Locate every Plasmodium ovale-infected red blood cell.
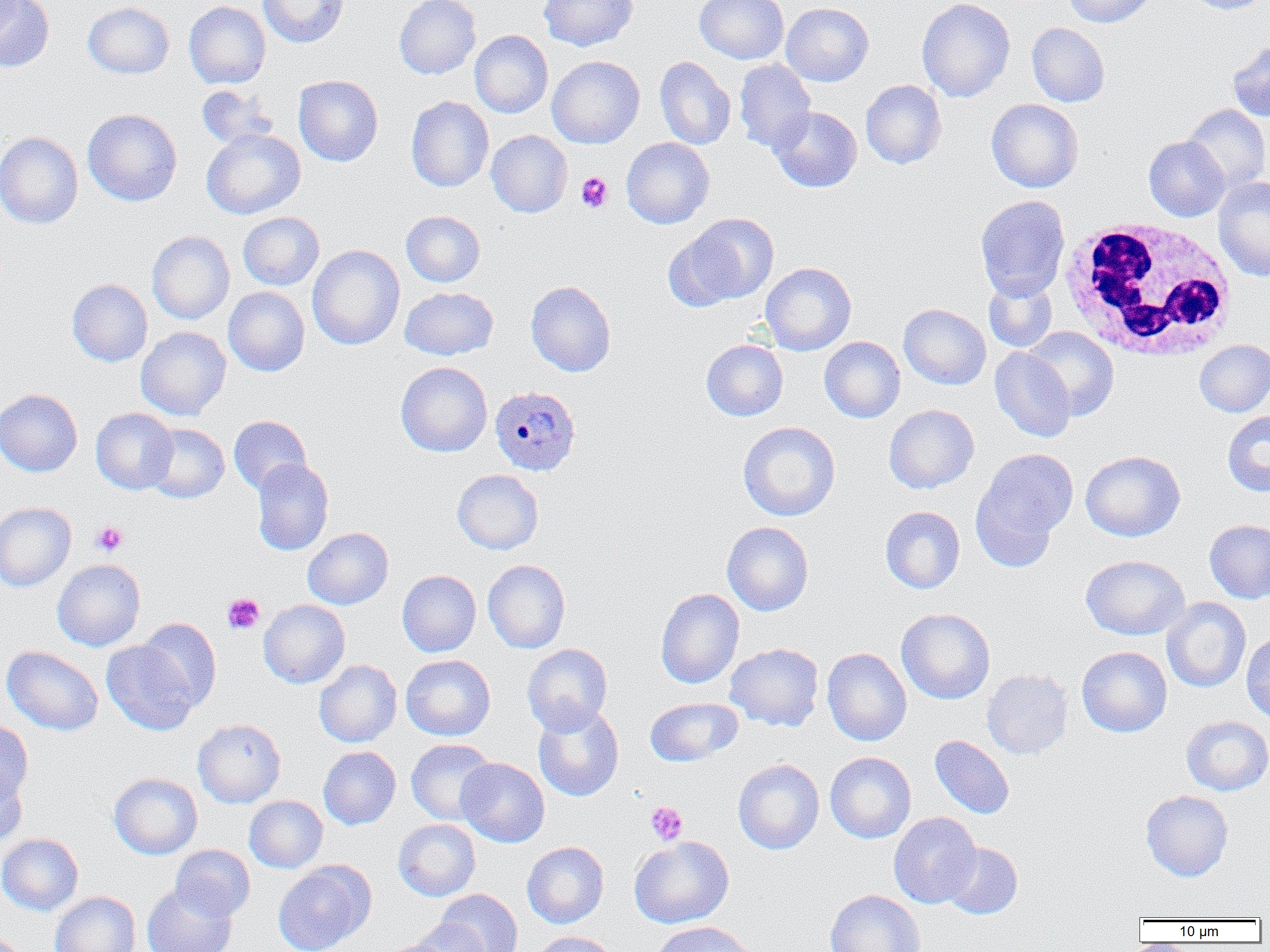

Approximate bounding boxes as (x1,y1)-(x2,y2) corner pairs in pixels.
Plasmodium ovale-infected red blood cells: (489,385)-(581,476).

White blood cell locations: (1058,218)-(1239,362). Platelet locations: (575,172)-(613,213), (91,520)-(128,556), (222,593)-(264,634), (645,801)-(687,845). Uninfected red blood cell locations: (0,0)-(54,73), (258,0)-(349,48), (394,0)-(481,79), (539,0)-(638,51), (694,0)-(789,64), (916,0)-(1015,103), (1062,0)-(1156,27), (1182,0)-(1270,15), (83,1)-(174,79), (184,1)-(271,88), (781,2)-(874,86), (1026,23)-(1109,107), (469,30)-(553,118), (1226,40)-(1270,122), (547,56)-(645,148), (654,56)-(736,150), (734,59)-(816,153), (293,75)-(383,166), (861,80)-(947,169), (196,85)-(280,150), (406,96)-(493,192), (986,99)-(1083,193), (1182,104)-(1270,192), (769,106)-(862,193), (82,109)-(182,206), (202,128)-(305,219), (486,130)-(572,218), (0,131)-(83,229), (1144,136)-(1230,221), (621,137)-(714,229), (1213,176)-(1270,281), (975,195)-(1070,300), (401,210)-(485,287), (238,211)-(324,290), (676,213)-(779,306), (147,230)-(235,325), (307,245)-(405,350), (760,262)-(856,355), (983,277)-(1057,353), (67,278)-(153,366), (526,280)-(616,377), (400,286)-(498,360), (223,287)-(310,376), (898,303)-(991,390), (136,326)-(231,420), (1024,326)-(1119,420), (819,336)-(905,423), (701,339)-(788,421), (1194,340)-(1270,417), (989,348)-(1076,442), (395,361)-(492,457), (0,388)-(83,476), (884,404)-(979,493), (91,408)-(178,494), (1222,411)-(1270,496), (228,415)-(312,495), (738,421)-(840,521), (143,423)-(229,503), (972,448)-(1078,563), (1080,450)-(1185,542), (251,458)-(333,556), (452,469)-(543,554), (0,502)-(76,591), (880,506)-(965,593), (1204,519)-(1270,603), (721,521)-(814,616), (303,527)-(393,609), (1081,555)-(1189,640), (52,558)-(145,651), (482,559)-(570,653), (397,570)-(481,657), (655,588)-(744,689), (1162,597)-(1250,693), (259,599)-(350,689), (896,608)-(995,704), (136,618)-(221,712), (1241,631)-(1270,724), (102,640)-(198,735), (521,643)-(613,735), (725,643)-(824,731), (2,645)-(103,736), (1076,646)-(1172,737), (822,648)-(912,746), (401,654)-(496,741), (314,659)-(402,747), (982,669)-(1073,759), (645,697)-(743,767), (533,703)-(624,802), (1181,715)-(1270,796), (192,718)-(286,808), (0,720)-(33,804), (929,735)-(1015,819), (406,738)-(498,826), (318,746)-(400,830), (825,752)-(916,843), (456,758)-(549,847), (732,759)-(824,854), (0,765)-(28,847), (109,772)-(202,859), (1140,790)-(1233,881), (244,795)-(328,873), (889,812)-(982,908), (393,819)-(480,901), (0,833)-(83,915), (629,836)-(734,928), (522,841)-(609,928), (941,842)-(1023,919), (170,844)-(255,921), (273,861)-(374,952), (141,884)-(237,952), (434,889)-(522,952), (825,889)-(925,952), (50,891)-(140,952), (412,918)-(491,952), (651,921)-(756,952), (529,931)-(621,952), (379,939)-(460,952). Slide-level diagnosis: Plasmodium ovale. Captured at 1000x magnification. Thin blood smear. Image is 1270×952 pixels. Light microscopy. One field of a larger specimen.